Identify the preparation type.
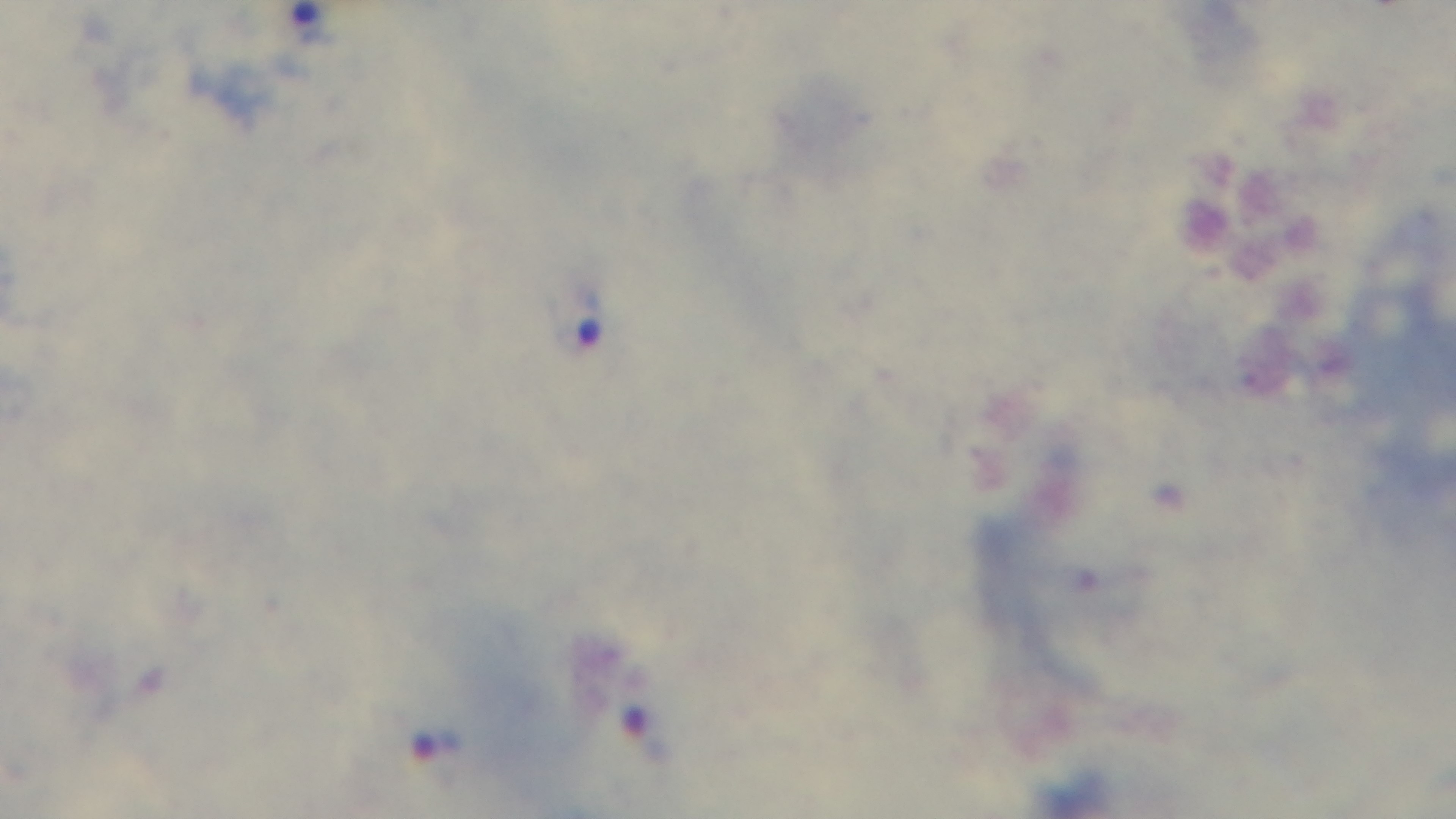
A thick smear.

Captured with a mounted 4K digital camera. 100x oil-immersion objective. One field from the slide. Malaria status: infected. Giemsa-stained. Photomicrograph.